Point out cells.
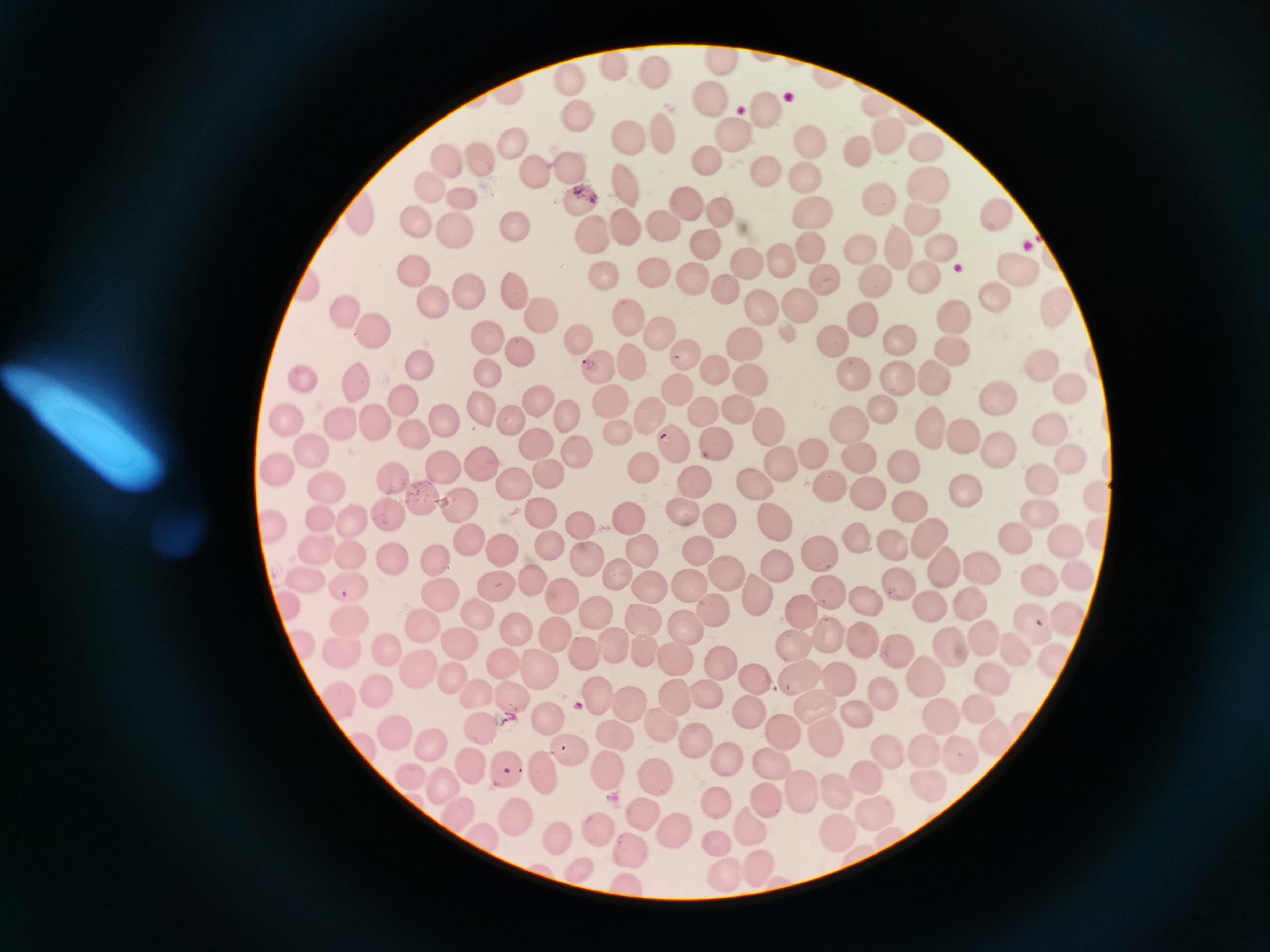

Approximate centers as {x, y} in pixels.
Cells: {721, 59}, {615, 64}, {655, 74}, {572, 81}, {510, 92}, {713, 100}, {880, 104}, {764, 111}, {580, 120}, {663, 132}, {731, 132}, {892, 140}, {628, 143}, {512, 144}, {808, 144}, {932, 145}, {860, 149}, {479, 156}, {446, 160}, {708, 160}, {569, 166}, {532, 169}, {768, 175}, {804, 179}, {925, 182}, {431, 187}, {624, 187}, {464, 201}, {689, 201}, {884, 201}, {580, 203}, {719, 212}, {362, 215}, {813, 215}, {661, 218}, {919, 218}, {997, 218}, {417, 222}, {624, 223}, {515, 225}, {452, 230}, {591, 238}, {712, 243}, {805, 244}, {937, 245}, {855, 249}, {900, 249}, {743, 259}, {778, 260}, {1014, 266}, {649, 267}, {413, 269}, {696, 274}, {921, 276}, {601, 279}, {823, 283}, {877, 285}, {307, 287}, {723, 287}, {510, 288}, {466, 290}, {995, 294}, {431, 303}, {759, 304}, {793, 304}, {1057, 306}, {350, 311}, {537, 316}, {953, 317}, {630, 320}, {864, 320}, {371, 329}, {484, 334}, {659, 335}, {577, 338}, {906, 339}, {836, 344}, {748, 346}, {952, 348}, {519, 349}, {680, 354}, {629, 357}, {1041, 361}, {421, 367}, {709, 368}, {600, 369}, {485, 370}, {894, 371}, {937, 374}, {301, 377}, {754, 377}, {359, 378}, {854, 380}, {1065, 386}, {679, 388}, {535, 396}, {406, 398}, {999, 398}, {611, 403}, {734, 408}, {884, 408}, {478, 409}, {564, 410}, {702, 411}, {651, 413}, {507, 418}, {763, 418}, {341, 420}, {287, 421}, {441, 421}, {372, 422}, {927, 425}, {408, 429}, {1046, 429}, {952, 430}, {853, 432}, {621, 437}, {711, 440}, {994, 443}, {533, 444}, {668, 444}, {313, 450}, {578, 453}, {1067, 455}, {809, 456}, {858, 458}, {779, 462}, {903, 464}, {486, 466}, {442, 467}, {282, 470}, {645, 472}, {550, 473}, {393, 477}, {691, 479}, {752, 480}, {1044, 480}, {516, 483}, {965, 488}, {327, 490}, {828, 490}, {1096, 493}, {864, 494}, {425, 499}, {906, 500}, {460, 504}, {1032, 508}, {539, 511}, {680, 511}, {392, 514}, {629, 517}, {716, 518}, {775, 519}, {354, 520}, {581, 525}, {273, 530}, {923, 534}, {1013, 535}, {850, 537}, {461, 538}, {547, 541}, {1066, 542}, {893, 543}, {640, 547}, {497, 548}, {816, 550}, {319, 552}, {583, 552}, {699, 554}, {349, 556}, {433, 557}, {390, 558}, {777, 560}, {946, 566}, {985, 570}, {620, 571}, {723, 572}, {1039, 574}, {1073, 577}, {308, 580}, {688, 583}, {346, 584}, {651, 584}, {896, 585}, {532, 587}, {496, 591}, {755, 593}, {828, 593}, {438, 594}, {291, 597}, {562, 597}, {861, 601}, {924, 603}, {963, 603}, {712, 612}, {799, 613}, {475, 614}, {596, 616}, {1065, 616}, {1028, 619}, {353, 620}, {422, 621}, {643, 625}, {682, 625}, {517, 629}, {978, 631}, {556, 635}, {832, 635}, {860, 636}, {304, 640}, {457, 643}, {951, 644}, {385, 647}, {797, 648}, {585, 649}, {896, 649}, {342, 650}, {613, 651}, {1017, 652}, {638, 656}, {1052, 658}, {673, 663}, {498, 664}, {719, 665}, {540, 668}, {417, 669}, {922, 675}, {989, 675}, {457, 678}, {800, 680}, {845, 680}, {754, 684}, {376, 688}, {476, 692}, {889, 692}, {599, 698}, {341, 699}, {705, 699}, {681, 701}, {626, 704}, {978, 705}, {512, 706}, {819, 706}, {935, 709}, {749, 710}, {858, 712}, {548, 716}, {661, 723}, {483, 730}, {393, 732}, {615, 735}, {823, 735}, {785, 737}, {991, 738}, {430, 742}, {694, 744}, {366, 745}, {572, 746}, {926, 749}, {887, 751}, {958, 751}, {722, 758}, {772, 760}, {604, 768}, {477, 769}, {508, 770}, {550, 773}, {863, 773}, {411, 779}, {655, 779}, {924, 781}, {446, 782}, {798, 788}, {838, 788}, {764, 797}, {716, 801}, {456, 810}, {873, 811}, {523, 816}, {645, 816}, {747, 827}, {836, 828}, {600, 830}, {482, 834}, {677, 834}, {557, 836}, {715, 838}, {632, 853}, {755, 866}, {580, 867}, {722, 878}, {616, 881}.

preparation = thin smear
image size = 1270×952 pixels
field of view = single
capture = smartphone camera at the microscope eyepiece
stain = Giemsa